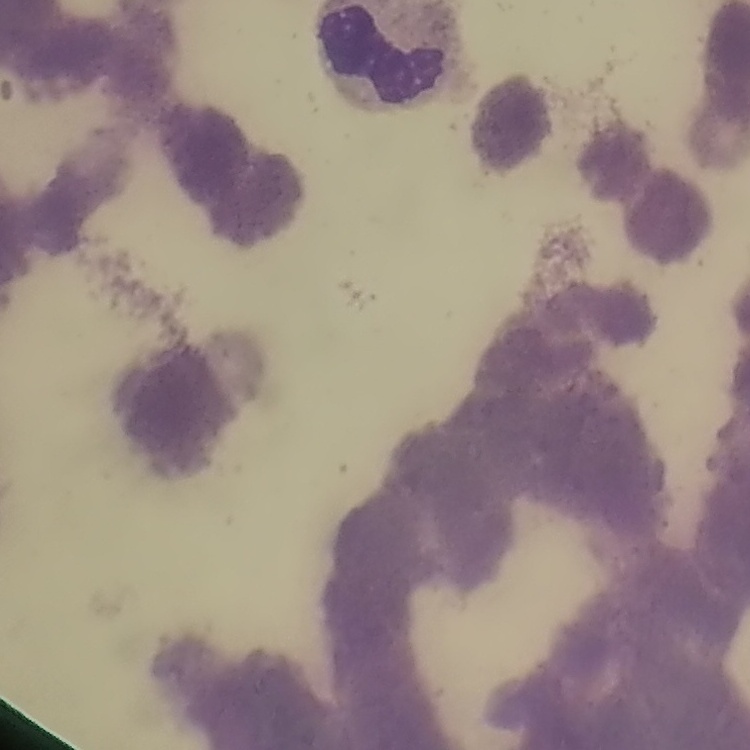
Summary:
  - Erythrocyte morphology: rouleaux formation
  - Image type: square crop of a larger photomicrograph
  - Preparation: thin peripheral smear
  - Stain: Field's or Giemsa